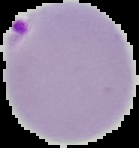
Summary:
  - Image size: 139×148 pixels
  - Image type: cell region segmented out of the field of view; surrounding area masked to black
  - Malaria status: parasitized
  - Preparation: thin blood film